Comment on the morphology of the erythrocytes.
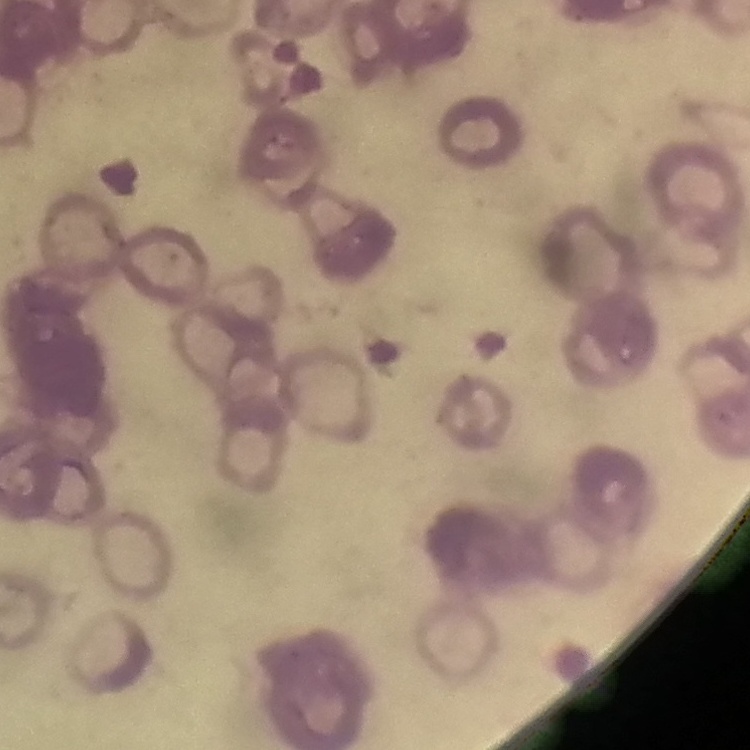
Rouleaux formation.

Summary:
  - Stain: Field's or Giemsa
  - Image type: one tile cut from a larger photomicrograph
  - Preparation: thin peripheral smear